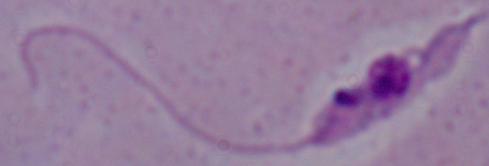
{
  "modality": "micrograph",
  "identification": "Leishmania",
  "magnification": "1000x"
}